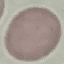 Malaria status: uninfected. Photographed with a smartphone camera at the microscope eyepiece. Giemsa stain. Cell patch, automatically extracted from a larger field of view and resized to 64 × 64 pixels. Thin blood smear.